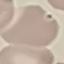

malaria status = uninfected
image type = cell patch, automatically extracted from a larger field of view and resized to 64 × 64 pixels
stain = Giemsa
capture = smartphone through the microscope eyepiece
preparation = thin blood smear